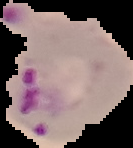
Image is 133×148 pixels. The area outside the segmented cell region is set to black. From a thin blood film. Result: malaria parasites identified.